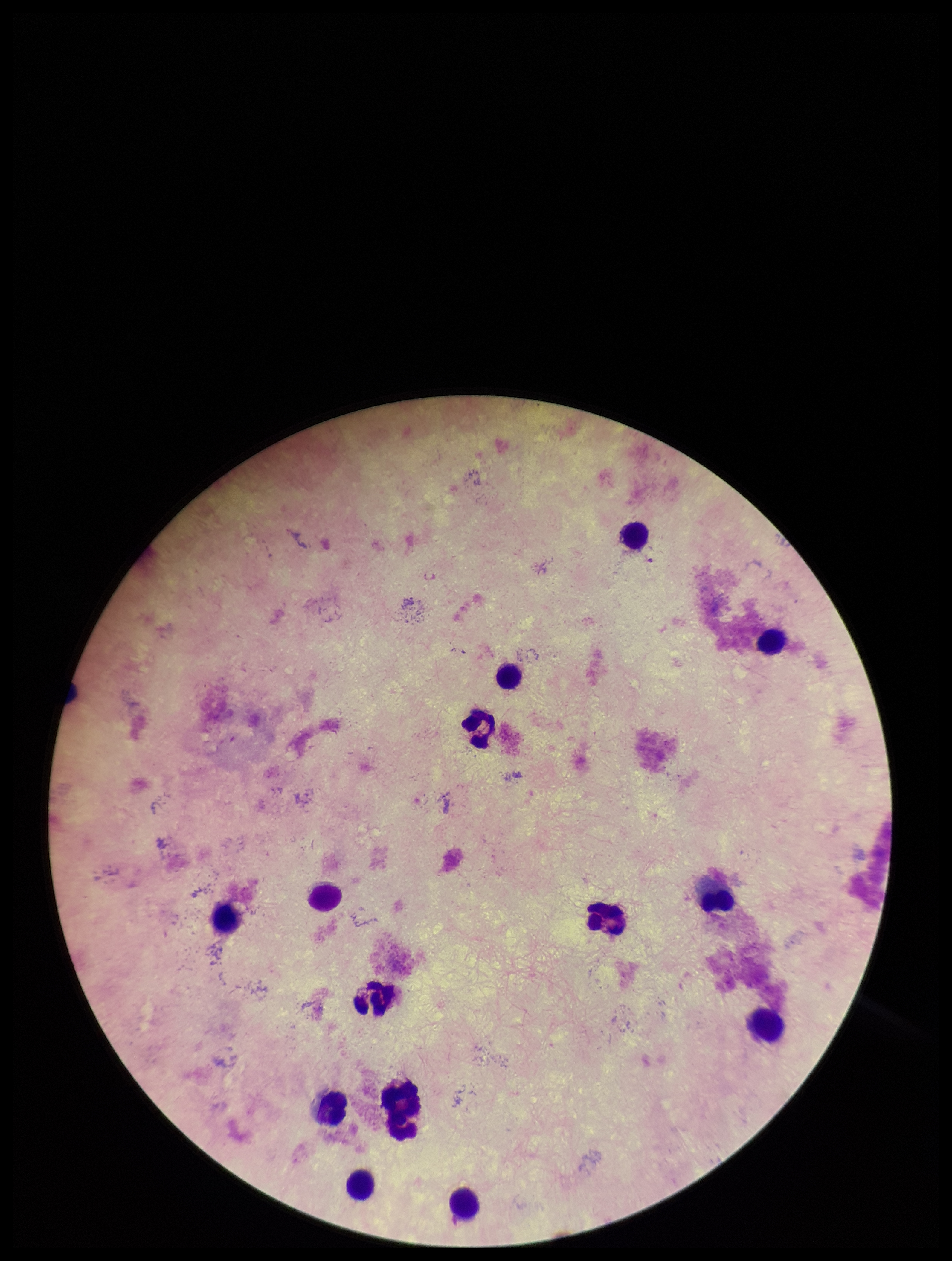

Patient malaria status: negative. Stained with Giemsa. Parasite count: 0. Leukocyte count: 14. Single field of view. Preparation: thick. Photographed through the microscope eyepiece with a smartphone camera. Image is 952×1261 pixels. Plasmodium parasites: none detected.